Identify the parasite.
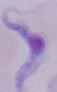

A trypanosome.

Photomicrograph. 1000x magnification.